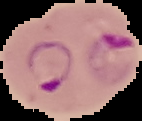
Malaria status: parasitized. Image is 142×121 pixels. From a thin blood film. Cell region segmented out of the field of view; the surrounding area is masked to black.